Locate every malaria parasite.
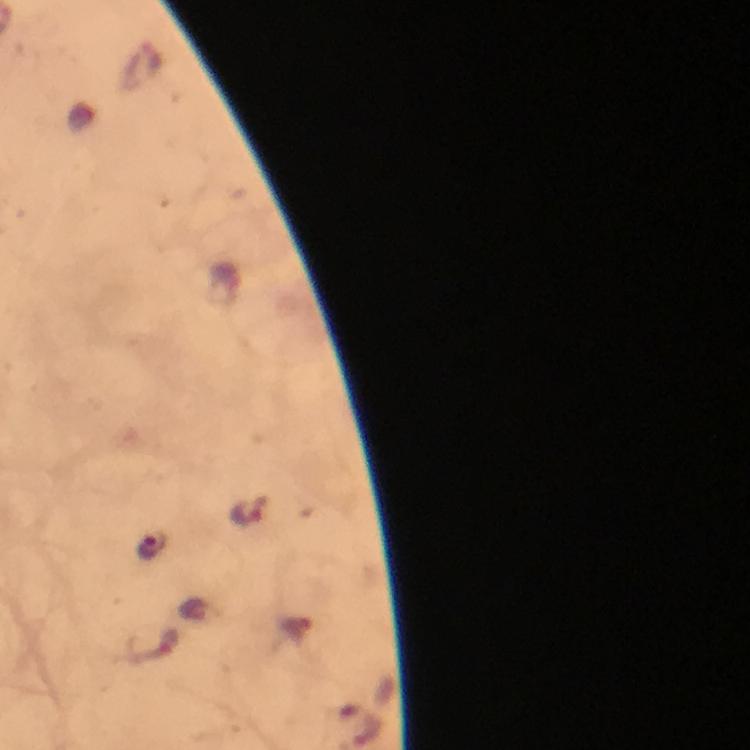

Approximate centers as [x, y] in pixels.
Malaria parasites: [249, 510], [151, 546].

capture: smartphone camera through the microscope
cropped_from: one field of view
stain: Giemsa
magnification: 100x
context: from a malaria diagnostic workup
preparation: thick smear
immersion_oil: applied
image_size: 750×750 pixels